Outline platelets.
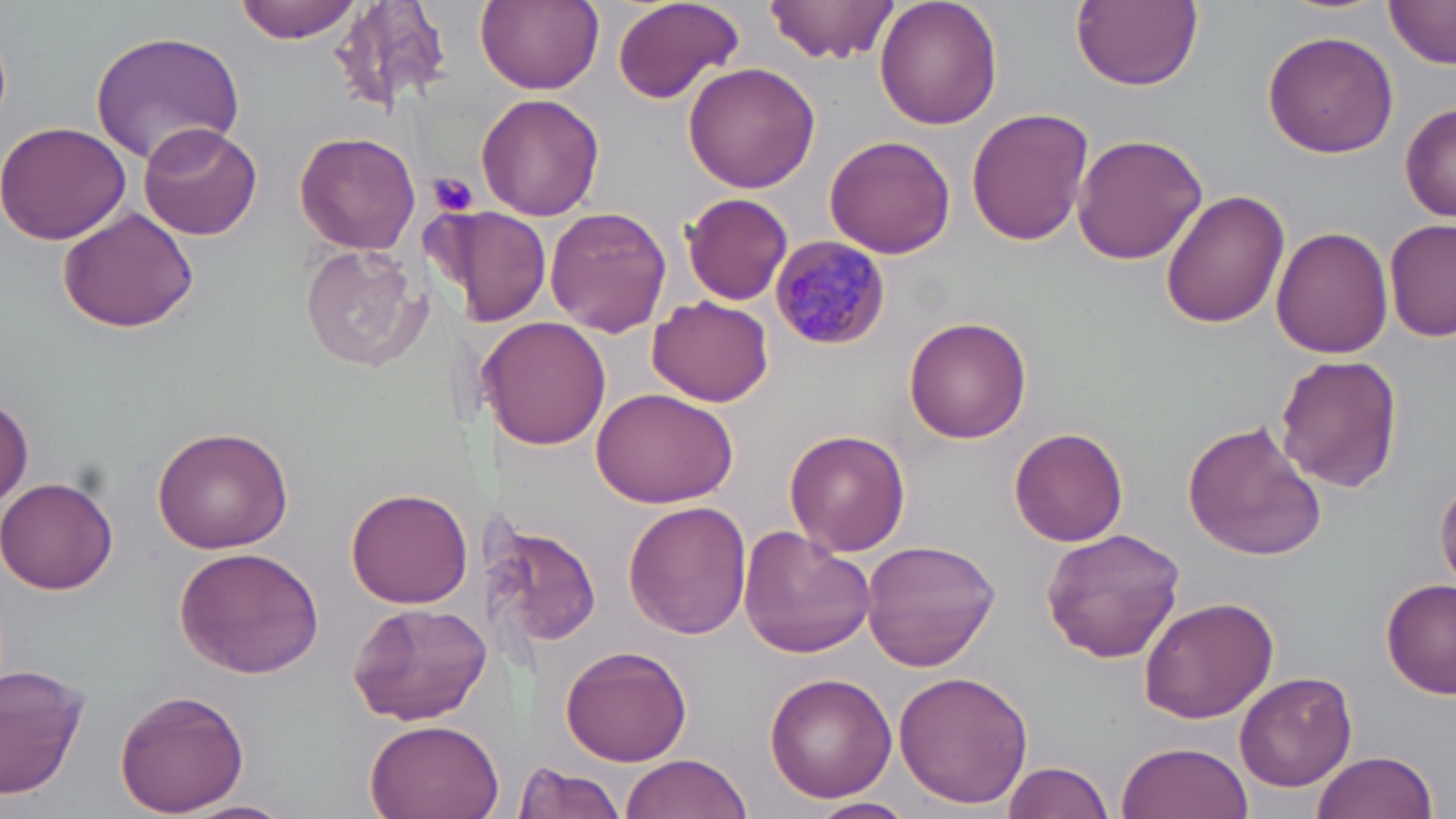
Approximate bounding boxes as (x1,y1)-(x2,y2) corner pairs in pixels.
Platelets: (425,171)-(480,220).

{
  "slide_level_diagnosis": "Plasmodium malariae",
  "magnification": "1000x",
  "plasmodium_malariae_infected_red_blood_cell_locations": "approximate bounding boxes as (x1,y1)-(x2,y2) corner pairs in pixels: (769,234)-(892,353)",
  "field_of_view": "one of a larger specimen",
  "preparation": "thin blood film",
  "modality": "light microscopy",
  "stain": "May-Grünwald-Giemsa",
  "image_size": "1456×819 pixels",
  "uninfected_red_blood_cell_locations": "approximate bounding boxes as (x1,y1)-(x2,y2) corner pairs in pixels: (235,0)-(366,45), (330,0)-(456,114), (474,0)-(603,92), (612,0)-(744,105), (764,0)-(899,65), (873,0)-(1003,130), (1072,0)-(1202,91), (1385,0)-(1456,67), (89,30)-(246,164), (1262,30)-(1399,159), (683,61)-(823,193), (473,94)-(605,220), (1401,101)-(1456,225), (966,106)-(1095,249), (0,120)-(133,247), (137,122)-(264,241), (294,129)-(420,255), (823,133)-(955,258), (1072,133)-(1207,265), (1161,190)-(1290,328), (683,193)-(794,306), (58,207)-(199,333), (450,207)-(550,328), (546,207)-(672,336), (1385,218)-(1455,344), (1273,225)-(1394,360), (297,242)-(432,373), (648,294)-(773,407), (481,316)-(611,451), (904,316)-(1033,442), (1276,353)-(1402,492), (591,385)-(737,508), (0,396)-(32,510), (1181,419)-(1327,562), (152,424)-(295,553), (1008,428)-(1129,547), (785,429)-(911,556), (0,474)-(121,594), (1435,476)-(1456,592), (344,486)-(472,607), (624,500)-(751,638), (502,517)-(601,651), (739,527)-(875,658), (1039,528)-(1186,663), (862,539)-(1001,671), (172,546)-(326,679), (1380,577)-(1455,700), (1139,594)-(1279,724), (346,600)-(492,726), (561,644)-(695,767), (0,665)-(87,798), (894,670)-(1033,809), (762,672)-(896,800), (1235,672)-(1357,793), (114,688)-(249,815), (360,718)-(504,819), (1116,739)-(1252,819), (1311,748)-(1439,819), (619,754)-(753,819), (1002,759)-(1117,819), (513,760)-(629,819), (809,797)-(916,819)"
}